Classify this cell by malaria status.
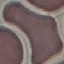
Uninfected.

Photographed with a smartphone camera at the microscope eyepiece. Thin blood film. Cell patch, automatically extracted from a larger field of view and resized to 64 × 64 pixels. Giemsa stain.